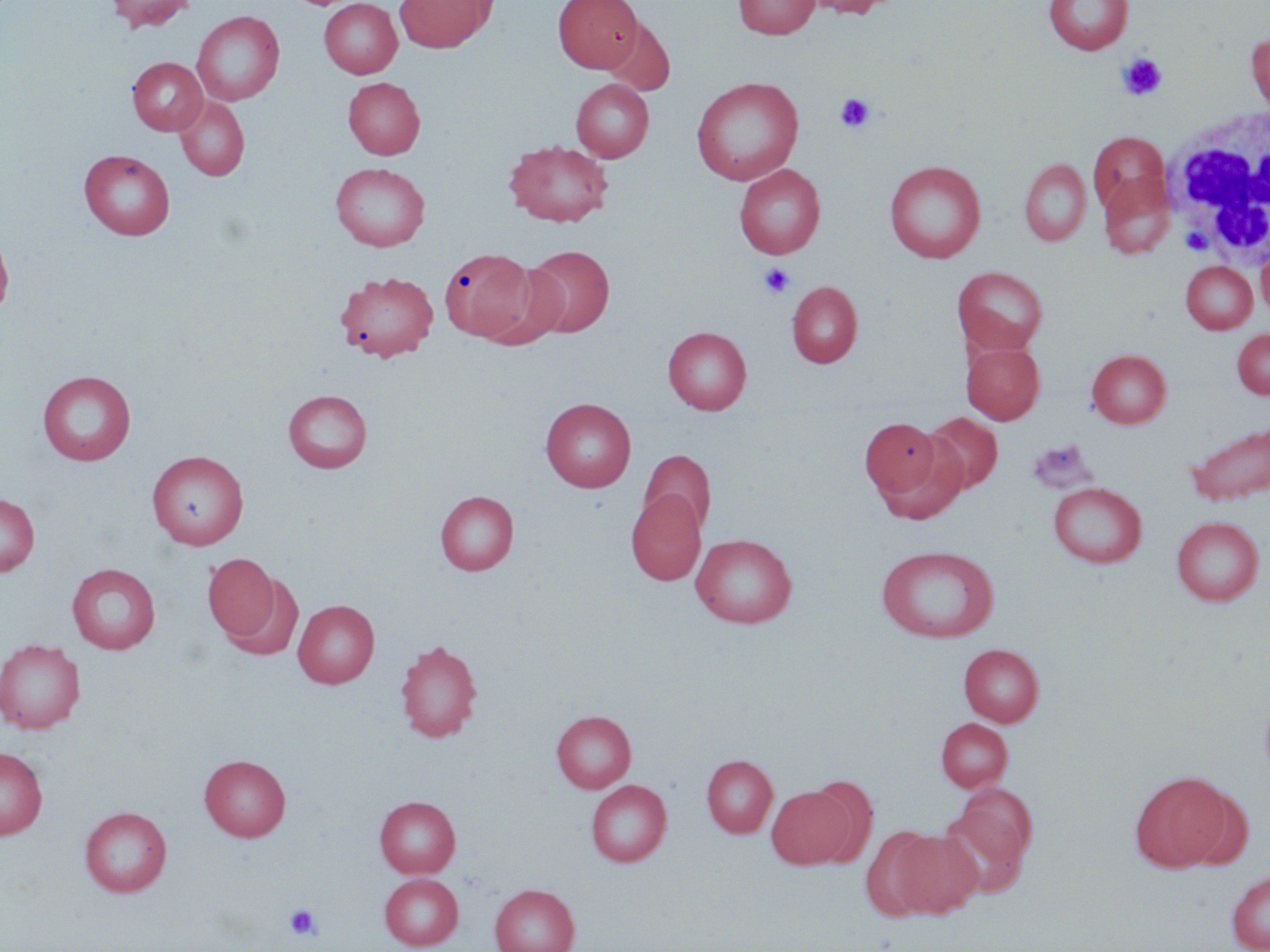
Approximate bounding boxes as named x1/y1/x2/y2 corners in pixels. Uninfected red blood cell locations: (x1=106, y1=0, x2=195, y2=32), (x1=394, y1=0, x2=495, y2=52), (x1=554, y1=0, x2=642, y2=72), (x1=733, y1=0, x2=819, y2=39), (x1=801, y1=0, x2=896, y2=18), (x1=1044, y1=0, x2=1133, y2=54), (x1=319, y1=1, x2=402, y2=78), (x1=192, y1=10, x2=285, y2=105), (x1=601, y1=18, x2=675, y2=96), (x1=1247, y1=33, x2=1270, y2=114), (x1=128, y1=57, x2=208, y2=135), (x1=690, y1=76, x2=804, y2=185), (x1=343, y1=77, x2=425, y2=159), (x1=570, y1=78, x2=653, y2=162), (x1=174, y1=96, x2=250, y2=181), (x1=1088, y1=132, x2=1170, y2=216), (x1=504, y1=140, x2=614, y2=226), (x1=79, y1=149, x2=175, y2=240), (x1=1020, y1=158, x2=1091, y2=246), (x1=884, y1=160, x2=986, y2=263), (x1=330, y1=162, x2=430, y2=251), (x1=734, y1=164, x2=825, y2=259), (x1=1099, y1=173, x2=1176, y2=259), (x1=0, y1=229, x2=14, y2=322), (x1=523, y1=245, x2=615, y2=337), (x1=1256, y1=246, x2=1270, y2=320), (x1=439, y1=248, x2=538, y2=342), (x1=480, y1=259, x2=570, y2=347), (x1=1180, y1=261, x2=1257, y2=334), (x1=952, y1=267, x2=1048, y2=355), (x1=334, y1=271, x2=439, y2=361), (x1=787, y1=281, x2=862, y2=368), (x1=663, y1=326, x2=752, y2=415), (x1=1232, y1=328, x2=1270, y2=399), (x1=962, y1=342, x2=1044, y2=423), (x1=1086, y1=349, x2=1171, y2=428), (x1=37, y1=370, x2=136, y2=465), (x1=283, y1=389, x2=372, y2=473), (x1=540, y1=397, x2=636, y2=492), (x1=924, y1=412, x2=1002, y2=494), (x1=860, y1=418, x2=944, y2=500), (x1=1185, y1=424, x2=1270, y2=505), (x1=875, y1=436, x2=970, y2=524), (x1=1026, y1=440, x2=1098, y2=495), (x1=147, y1=450, x2=248, y2=549), (x1=639, y1=450, x2=716, y2=534), (x1=1048, y1=481, x2=1146, y2=568), (x1=435, y1=490, x2=519, y2=575), (x1=626, y1=490, x2=706, y2=585), (x1=0, y1=493, x2=39, y2=577), (x1=1171, y1=516, x2=1264, y2=606), (x1=690, y1=533, x2=797, y2=628), (x1=875, y1=545, x2=999, y2=643), (x1=203, y1=553, x2=279, y2=642), (x1=67, y1=562, x2=160, y2=653), (x1=222, y1=573, x2=304, y2=662), (x1=293, y1=599, x2=379, y2=688), (x1=0, y1=639, x2=86, y2=735), (x1=394, y1=639, x2=483, y2=743), (x1=959, y1=643, x2=1043, y2=727), (x1=551, y1=710, x2=636, y2=793), (x1=936, y1=717, x2=1012, y2=791), (x1=0, y1=746, x2=48, y2=839), (x1=199, y1=754, x2=291, y2=841), (x1=702, y1=754, x2=777, y2=838), (x1=1130, y1=772, x2=1229, y2=871), (x1=586, y1=780, x2=671, y2=866), (x1=766, y1=784, x2=854, y2=870), (x1=1179, y1=786, x2=1253, y2=871), (x1=939, y1=789, x2=1036, y2=893), (x1=375, y1=796, x2=460, y2=877), (x1=80, y1=806, x2=172, y2=897), (x1=860, y1=825, x2=941, y2=920), (x1=888, y1=830, x2=983, y2=918), (x1=1227, y1=870, x2=1270, y2=952), (x1=380, y1=873, x2=463, y2=950), (x1=490, y1=884, x2=580, y2=952). Platelet locations: (x1=1117, y1=53, x2=1167, y2=100), (x1=835, y1=93, x2=875, y2=132), (x1=759, y1=263, x2=795, y2=298), (x1=285, y1=903, x2=321, y2=941). White blood cell locations: (x1=1162, y1=108, x2=1270, y2=272). Slide-level diagnosis: negative for blood parasites. One field of a larger specimen. Thin blood film. 1000x magnification. Image is 1270×952 pixels. May-Grünwald-Giemsa-stained preparation. Light microscopy.